Assess this cell for malaria.
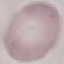
Uninfected.

Summary:
  - Capture: smartphone through the microscope eyepiece
  - Preparation: thin smear
  - Image type: cell patch, automatically extracted from a larger field of view and resized to 64 × 64 pixels
  - Stain: Giemsa